Report the malaria status of this cell.
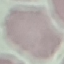
It is uninfected.

capture: smartphone through the microscope eyepiece
preparation: thin blood smear
image_type: automatically extracted cell patch, resized to 64 × 64 pixels
stain: Giemsa